Report the malaria status.
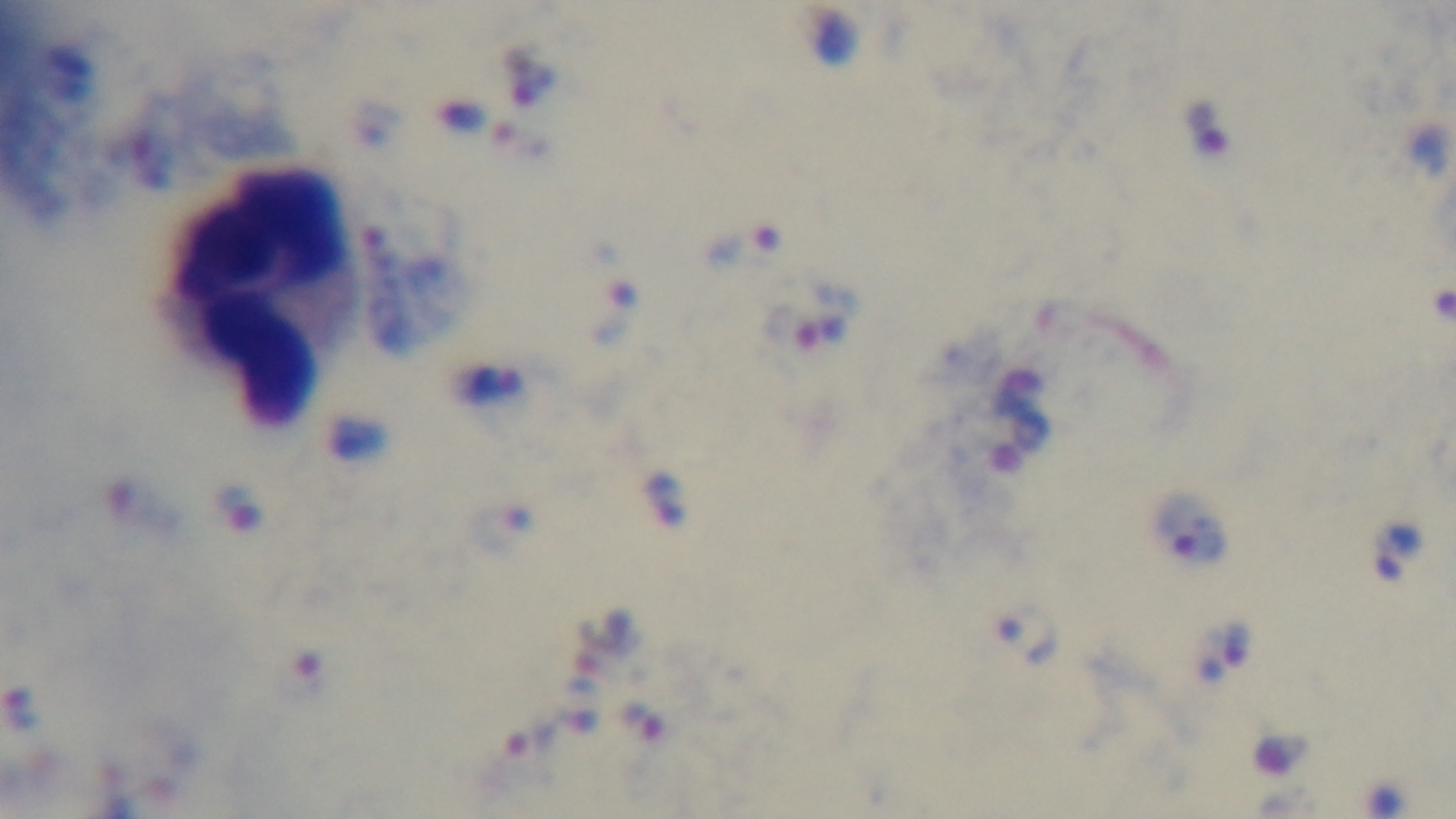

Positive.

objective = 100x oil immersion
field of view = single
capture = mounted 4K digital camera
modality = light microscopy
stain = Giemsa
preparation = thick